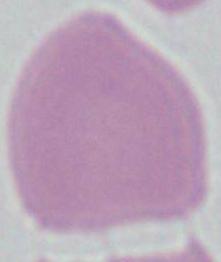 Photomicrograph. An erythrocyte is shown. Captured at 1000x magnification.